Locate and identify every blood parasite.
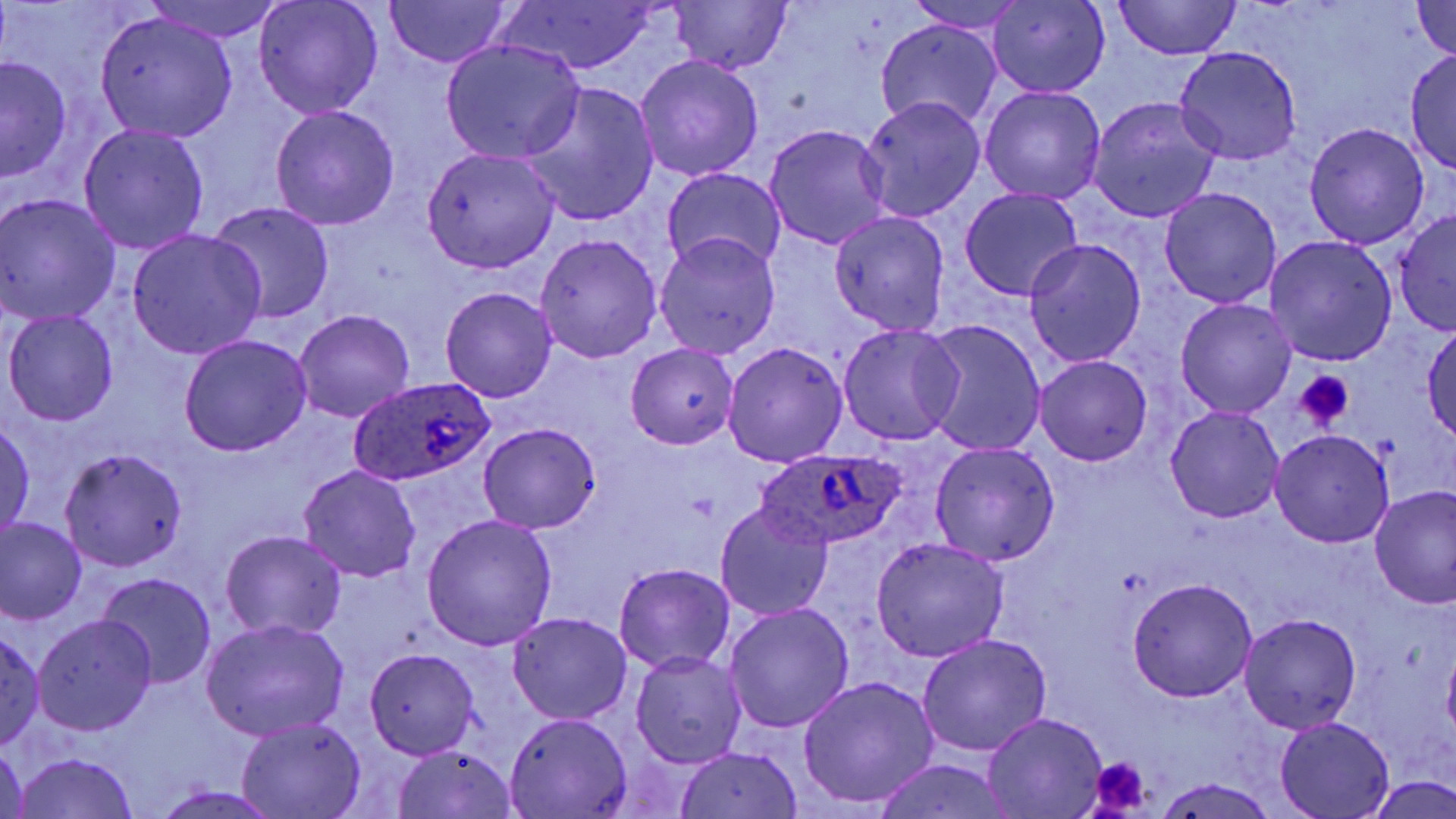
Approximate bounding boxes as (x1,y1)-(x2,y2) corner pairs in pixels.
Plasmodium ovale-infected red blood cells: (347,378)-(497,488), (753,448)-(906,550).
No Plasmodium falciparum, Plasmodium malariae, Plasmodium vivax, Babesia divergens, or Trypanosoma brucei observed.

slide-level diagnosis = Plasmodium ovale
platelet locations = approximate bounding boxes as (x1,y1)-(x2,y2) corner pairs in pixels: (1293,370)-(1356,431), (686,491)-(718,522), (1087,757)-(1153,813)
uninfected red blood cell locations = approximate bounding boxes as (x1,y1)-(x2,y2) corner pairs in pixels: (145,0)-(287,40), (253,0)-(384,120), (381,0)-(513,69), (494,0)-(663,75), (1109,0)-(1242,62), (668,1)-(791,74), (907,1)-(1030,34), (1412,1)-(1456,63), (987,3)-(1110,99), (90,13)-(239,142), (875,19)-(1002,132), (440,38)-(586,164), (1174,47)-(1303,166), (1407,49)-(1456,175), (0,54)-(73,182), (634,55)-(763,182), (516,84)-(660,227), (979,85)-(1107,205), (857,96)-(987,223), (1087,97)-(1221,223), (270,105)-(400,231), (1303,122)-(1430,249), (79,123)-(210,255), (763,123)-(892,251), (421,148)-(560,273), (661,167)-(787,276), (1159,187)-(1282,309), (959,188)-(1083,301), (0,195)-(122,326), (209,200)-(337,325), (1392,210)-(1456,338), (829,211)-(950,336), (124,228)-(266,360), (534,233)-(663,362), (653,234)-(781,359), (1264,235)-(1397,366), (1024,240)-(1146,366), (440,286)-(558,402), (1176,299)-(1297,419), (3,309)-(119,427), (294,309)-(415,422), (918,319)-(1047,456), (1422,320)-(1456,442), (837,322)-(964,447), (179,334)-(311,457), (723,342)-(848,468), (625,344)-(738,450), (1035,354)-(1152,465), (1165,405)-(1286,524), (1,420)-(35,539), (478,422)-(601,534), (1270,429)-(1395,547), (928,442)-(1060,566), (61,448)-(187,572), (297,466)-(421,583), (1370,486)-(1456,609), (714,505)-(833,621), (420,514)-(558,652), (1,519)-(87,622), (220,529)-(348,642), (870,538)-(1008,662), (614,563)-(736,675), (98,571)-(217,689), (1126,577)-(1259,701), (725,602)-(855,732), (507,612)-(633,725), (1239,613)-(1363,734), (33,615)-(157,735), (201,619)-(350,742), (0,628)-(46,752), (918,633)-(1051,758), (365,648)-(480,758), (630,652)-(747,768), (798,676)-(939,810), (983,711)-(1107,817), (505,713)-(634,817), (235,717)-(367,819), (1276,718)-(1396,817), (1,743)-(30,819), (392,746)-(520,819), (673,746)-(805,819), (14,752)-(139,819), (872,761)-(1020,819), (1366,775)-(1456,818), (1155,776)-(1280,818), (149,785)-(283,818)
stain = May-Grünwald-Giemsa
preparation = thin blood smear
field of view = one of a larger specimen
magnification = 1000x
modality = optical microscopy
image size = 1456×819 pixels